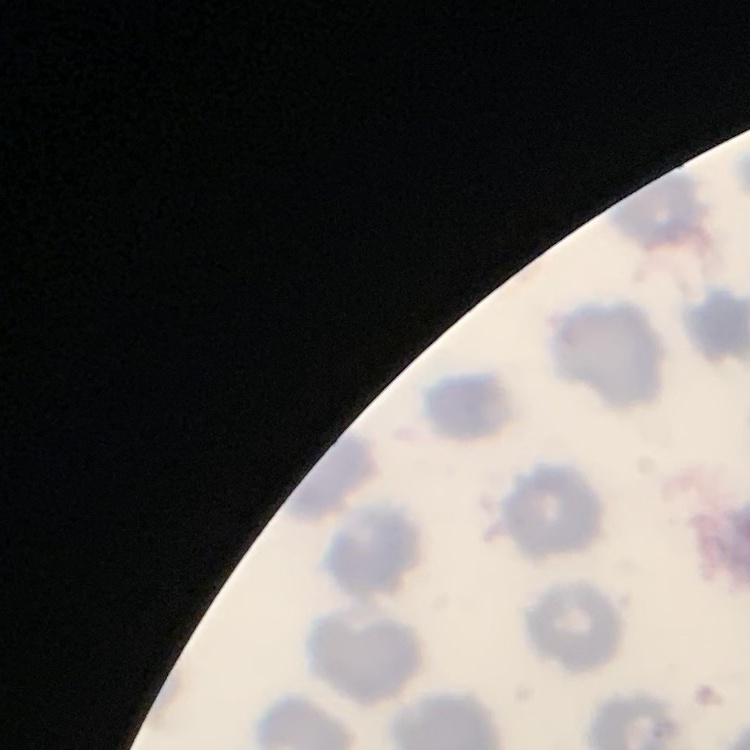

The erythrocytes exhibit no rouleaux formation. Thin blood film. Square crop of a larger photomicrograph. Field's or Giemsa stain.